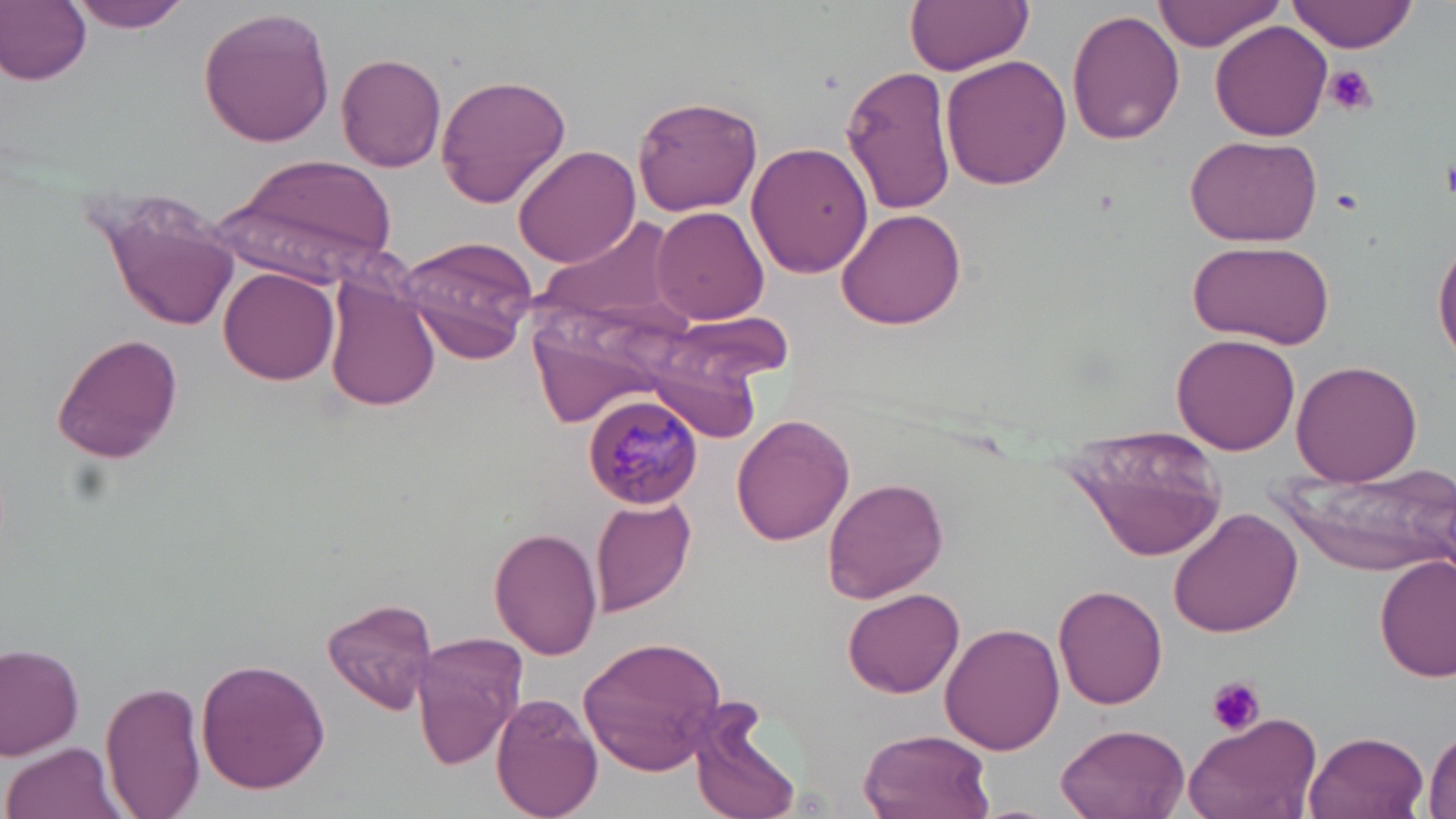

Summary:
  - Coordinate format: approximate bounding boxes as (x1,y1)-(x2,y2) corner pairs in pixels
  - Platelet locations: (1323,64)-(1378,117), (1442,154)-(1456,201), (1330,188)-(1365,215), (1208,677)-(1265,737)
  - Plasmodium malariae-infected red blood cell locations: (584,391)-(702,511)
  - Uninfected red blood cell locations: (0,0)-(91,84), (65,0)-(193,33), (906,0)-(1032,74), (1154,0)-(1281,52), (1291,0)-(1420,52), (196,6)-(336,147), (1063,9)-(1184,144), (1211,20)-(1333,142), (336,52)-(448,171), (941,56)-(1072,191), (841,64)-(956,215), (435,73)-(571,208), (632,94)-(764,215), (1184,134)-(1324,245), (512,143)-(640,268), (746,143)-(873,281), (223,150)-(399,283), (94,187)-(241,332), (651,206)-(769,324), (835,207)-(967,330), (539,218)-(686,328), (401,236)-(536,365), (1435,238)-(1456,369), (1185,239)-(1335,348), (220,267)-(339,384), (325,276)-(442,411), (654,317)-(785,414), (52,333)-(184,463), (1172,334)-(1301,456), (650,350)-(762,441), (1292,358)-(1423,485), (731,413)-(856,546), (1063,424)-(1229,561), (1276,460)-(1452,578), (823,476)-(949,603), (591,497)-(695,619), (1167,507)-(1304,637), (489,526)-(601,659), (1374,554)-(1455,683), (844,585)-(962,697), (1053,585)-(1168,709), (320,595)-(439,716), (942,622)-(1066,756), (411,630)-(527,765), (577,636)-(729,776), (0,642)-(83,756), (195,656)-(331,795), (101,680)-(209,819), (493,692)-(604,819), (688,703)-(805,819), (1184,710)-(1322,819), (1055,724)-(1190,819), (1426,727)-(1456,819), (860,729)-(993,819), (1303,730)-(1429,819), (4,740)-(124,819)
  - Slide-level diagnosis: Plasmodium malariae
  - Magnification: 1000x
  - Preparation: thin blood film
  - Modality: light microscopy
  - Image size: 1456×819 pixels
  - Stain: May-Grünwald-Giemsa
  - Field of view: single